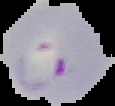
image_size: 115×106 pixels
image_type: cell region segmented out of the field of view; surrounding area masked to black
result: malaria parasites identified
preparation: thin blood smear